Assess this cell for malaria.
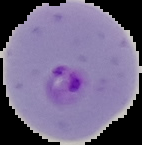

Parasitized.

From a thin blood film. Segmented cell region on a black background. Image is 142×145 pixels.